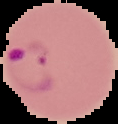
image size = 118×124 pixels
image type = segmented cell region with the area outside set to black
preparation = thin blood smear
result = malaria parasites identified